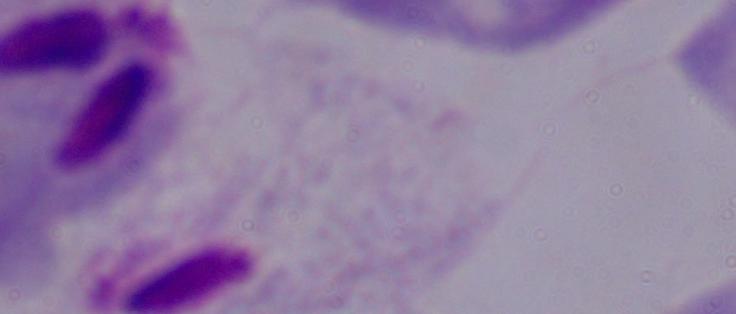
magnification = 1000x
modality = photomicrograph
identification = trichomonad